Locate and identify every blood parasite.
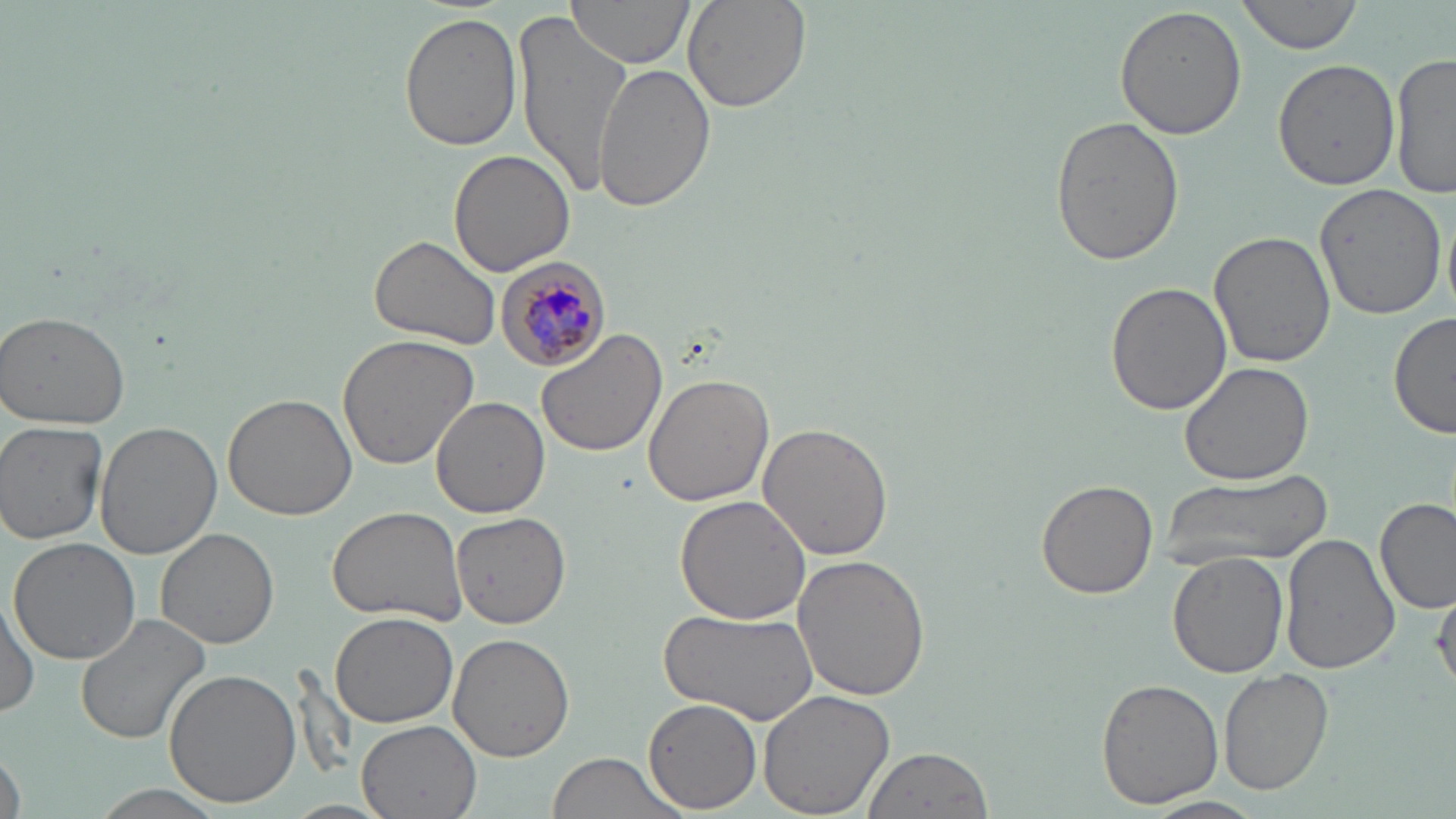
Approximate bounding boxes as [x1, y1, x2, y2] in pixels.
Plasmodium malariae-infected red blood cells: [493, 255, 614, 371].
No Plasmodium falciparum, Plasmodium ovale, Plasmodium vivax, Babesia divergens, or Trypanosoma brucei observed.

slide_level_diagnosis: Plasmodium malariae
preparation: thin blood smear
uninfected_red_blood_cell_locations: 'approximate bounding boxes as [x1, y1, x2, y2] in pixels: [564, 0, 694, 71], [681, 0, 812, 115], [1236, 0, 1365, 54], [1113, 5, 1248, 141], [515, 9, 630, 197], [399, 13, 523, 151], [1391, 51, 1456, 198], [1273, 60, 1402, 190], [593, 62, 716, 213], [1049, 116, 1184, 266], [449, 150, 576, 278], [1313, 182, 1445, 320], [1209, 230, 1336, 369], [368, 233, 500, 351], [1105, 282, 1232, 416], [1, 310, 131, 431], [1389, 311, 1456, 441], [537, 329, 667, 458], [337, 333, 482, 470], [1179, 359, 1316, 484], [642, 372, 772, 506], [224, 393, 358, 521], [432, 396, 548, 518], [93, 419, 222, 559], [1, 420, 108, 545], [758, 423, 895, 560], [1165, 473, 1325, 570], [1036, 480, 1158, 599], [675, 496, 811, 625], [1374, 497, 1455, 615], [328, 504, 470, 625], [452, 509, 572, 629], [154, 527, 279, 649], [1280, 533, 1398, 675], [9, 538, 141, 664], [1167, 551, 1291, 680], [792, 555, 932, 701], [1432, 585, 1456, 694], [0, 594, 38, 720], [655, 606, 821, 724], [330, 610, 458, 729], [73, 613, 212, 743], [447, 634, 574, 761], [1218, 668, 1332, 795], [164, 669, 301, 807], [1094, 678, 1224, 809], [757, 686, 896, 817], [644, 697, 763, 815], [357, 718, 483, 819], [1, 745, 26, 819], [862, 746, 993, 819], [542, 752, 692, 819], [90, 785, 226, 817], [1139, 797, 1271, 819], [279, 798, 396, 818]'
image_size: 1456×819 pixels
magnification: 1000x
field_of_view: single
stain: May-Grünwald-Giemsa
modality: light microscopy